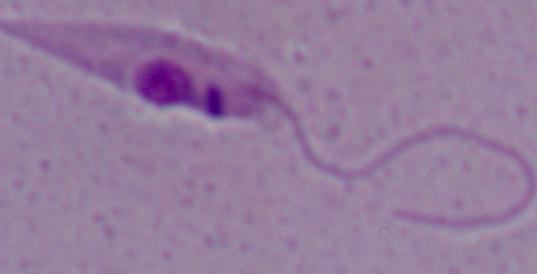

Summary:
  - Modality: micrograph
  - Magnification: 1000x
  - Identification: Leishmania